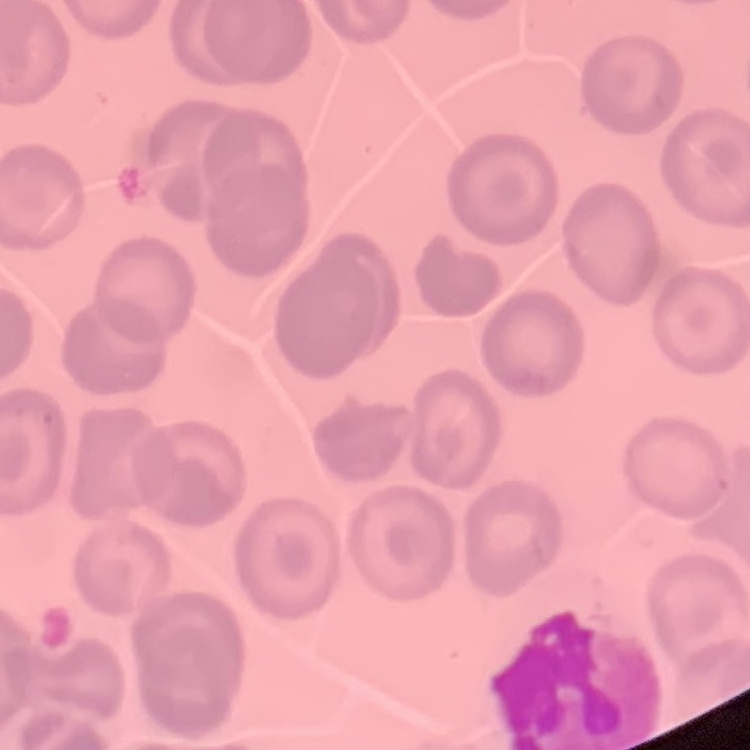
red_blood_cell_morphology: no rouleaux formation
image_type: one tile cut from a larger photomicrograph
stain: Field's or Giemsa
preparation: thin blood film